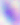

Summary:
  - Modality: photomicrograph
  - Identification: Toxoplasma gondii
  - Magnification: 400x